Give a bounding box for every Plasmodium parasite, every leukocyte, and every artifact (stain precipitate or debris).
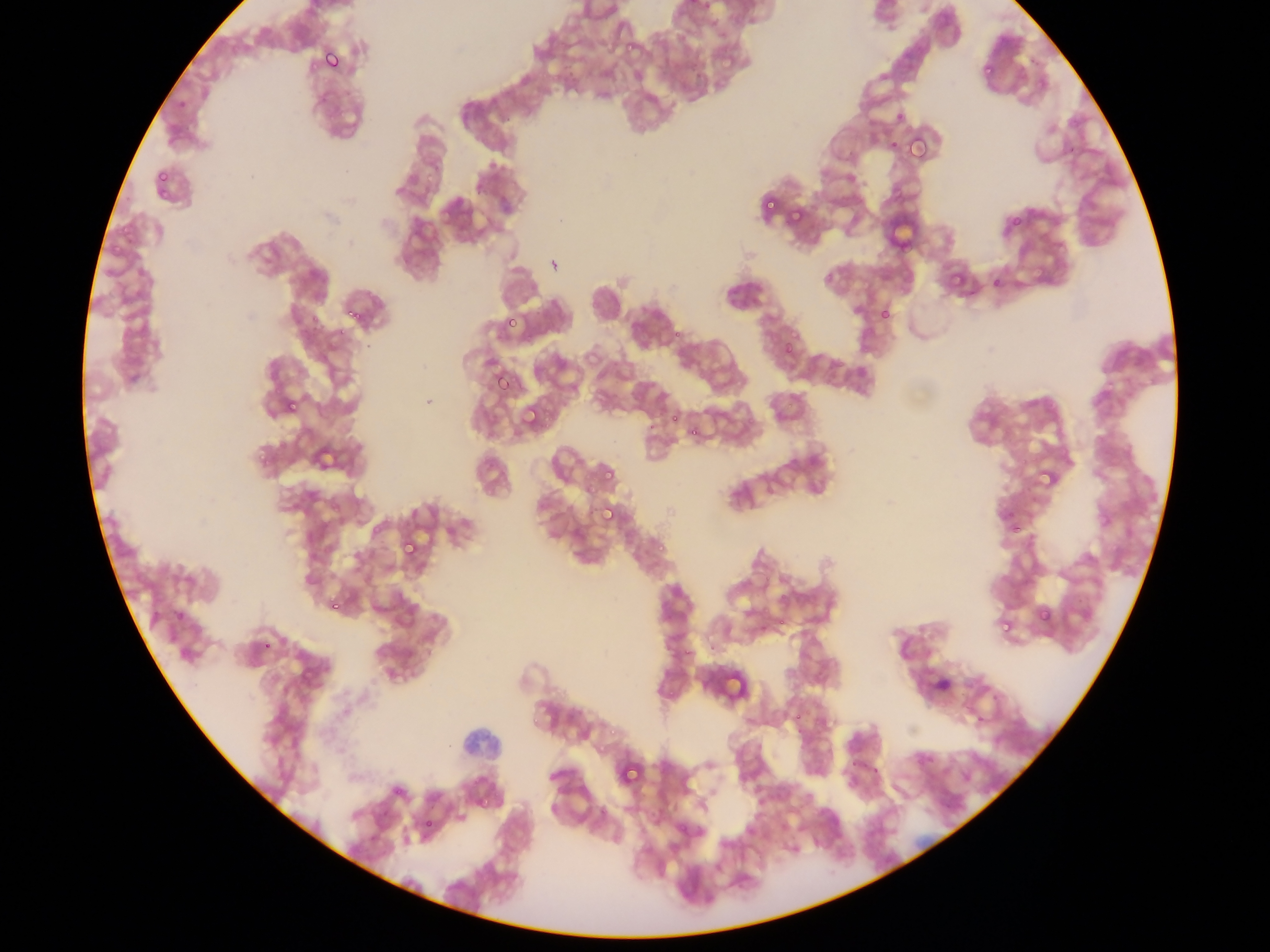
Approximate bounding boxes as {left, top, right, bottom} in pixels.
Plasmodium parasites: {620, 35, 637, 52}, {317, 45, 347, 76}, {977, 59, 998, 75}, {906, 134, 930, 162}, {888, 144, 901, 155}, {156, 167, 176, 190}, {159, 181, 182, 197}, {892, 190, 906, 201}, {762, 196, 780, 215}, {789, 202, 810, 224}, {995, 221, 1019, 241}, {106, 237, 129, 254}, {986, 271, 1007, 288}, {946, 274, 957, 288}, {345, 304, 368, 327}, {876, 304, 894, 324}, {308, 307, 319, 324}, {506, 318, 520, 329}, {331, 322, 348, 336}, {781, 343, 795, 354}, {489, 369, 513, 395}, {283, 399, 300, 416}, {520, 403, 545, 432}, {667, 411, 678, 424}, {691, 424, 710, 434}, {256, 438, 278, 464}, {1034, 462, 1057, 488}, {603, 465, 613, 482}, {598, 503, 620, 526}, {1001, 506, 1024, 534}, {399, 536, 420, 562}, {654, 543, 662, 551}, {326, 596, 344, 619}, {1034, 605, 1053, 625}, {172, 606, 189, 624}, {998, 616, 1010, 631}, {260, 633, 274, 653}, {716, 662, 745, 694}, {791, 706, 812, 722}, {604, 721, 616, 733}, {616, 759, 644, 790}, {479, 791, 498, 807}, {424, 811, 439, 828}.
No leukocytes observed.

Summary:
  - Field of view: single
  - Preparation: thin blood smear
  - Capture: mobile-phone photograph through a microscope
  - Image size: 1270×952 pixels
  - Country: Ghana